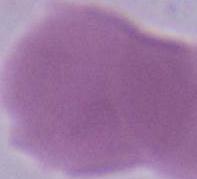
Summary:
  - Modality: photomicrograph
  - Magnification: 1000x
  - Identification: red blood cell